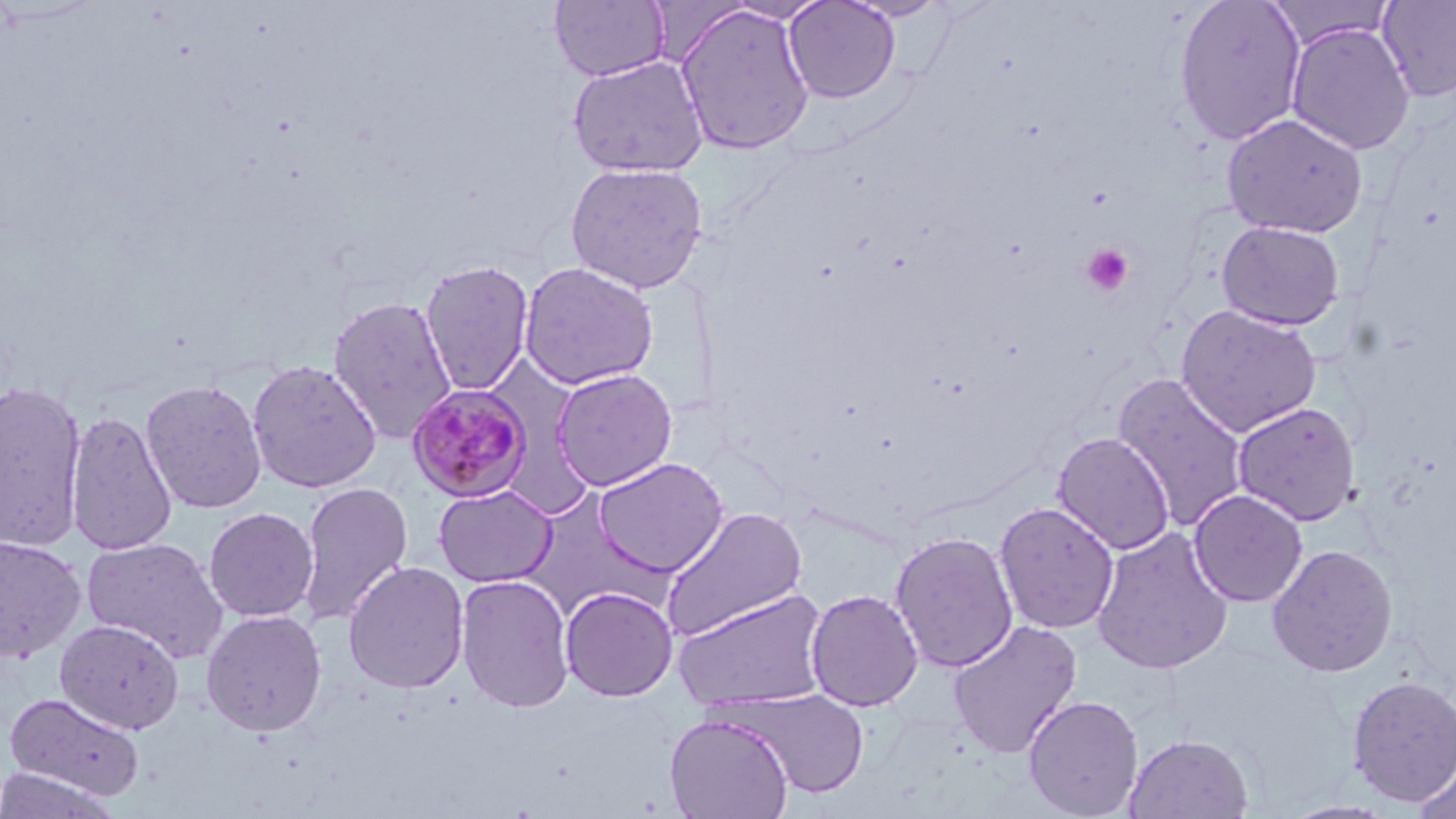

slide-level diagnosis = Plasmodium malariae
platelet locations = approximate bounding boxes as [x1, y1, x2, y2] in pixels: [1081, 243, 1134, 296]
magnification = 1000x
uninfected red blood cell locations = approximate bounding boxes as [x1, y1, x2, y2] in pixels: [784, 0, 900, 103], [845, 0, 946, 20], [1174, 0, 1307, 146], [1265, 0, 1396, 49], [550, 1, 670, 82], [1378, 1, 1456, 103], [674, 3, 815, 156], [1286, 22, 1415, 155], [567, 55, 709, 177], [1222, 113, 1368, 238], [565, 162, 709, 294], [1217, 221, 1345, 330], [419, 259, 535, 397], [518, 260, 659, 391], [327, 296, 458, 445], [1175, 305, 1323, 437], [246, 359, 382, 493], [552, 368, 677, 492], [1113, 374, 1250, 534], [140, 378, 268, 514], [0, 379, 88, 553], [1232, 402, 1360, 526], [65, 409, 177, 556], [1052, 432, 1175, 555], [593, 457, 728, 576], [298, 482, 413, 627], [433, 484, 557, 587], [1189, 490, 1308, 607], [994, 503, 1120, 634], [659, 506, 808, 643], [203, 507, 319, 622], [1092, 527, 1233, 676], [890, 531, 1019, 674], [0, 535, 86, 663], [82, 537, 229, 661], [1267, 544, 1398, 677], [343, 561, 470, 694], [456, 574, 575, 713], [559, 586, 678, 702], [673, 589, 830, 711], [805, 589, 924, 712], [201, 609, 327, 737], [56, 619, 184, 734], [947, 619, 1083, 759], [1348, 674, 1456, 805], [729, 687, 870, 797], [3, 691, 146, 800], [1023, 695, 1144, 818], [664, 713, 794, 819], [1125, 733, 1254, 818], [1411, 758, 1456, 819], [0, 767, 121, 818], [1281, 800, 1397, 818]
preparation = thin blood smear
field of view = single
stain = May-Grünwald-Giemsa
image size = 1456×819 pixels
Plasmodium malariae-infected red blood cell locations = approximate bounding boxes as [x1, y1, x2, y2] in pixels: [406, 382, 533, 503]
modality = optical microscopy